Locate every Plasmodium parasite.
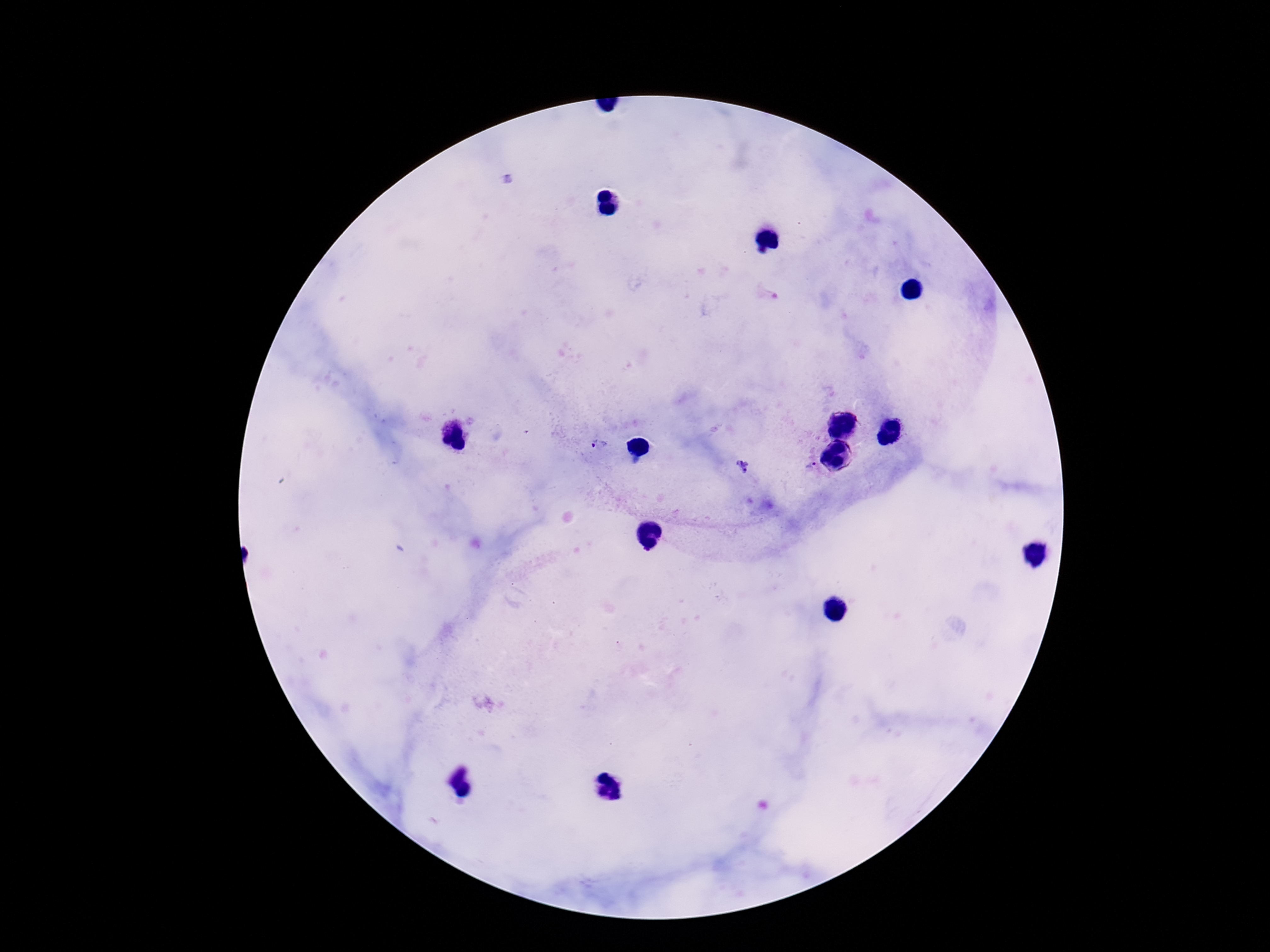
Approximate object centers, in pixels from the top-left corner.
Plasmodium parasites: (x=599, y=444), (x=743, y=467), (x=811, y=467).

capture = smartphone camera through the microscope eyepiece
stain = Giemsa
patient malaria status = infected
preparation = thick peripheral-blood smear
magnification = 100x
image size = 1270×952 pixels
field of view = single